Name the parasite shown.
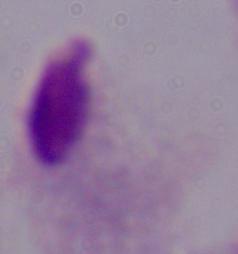

This is a trichomonad.

Summary:
  - Modality: micrograph
  - Magnification: 1000x